Identify the parasite.
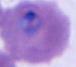

Plasmodium.

modality = micrograph
magnification = 400x or 1000x